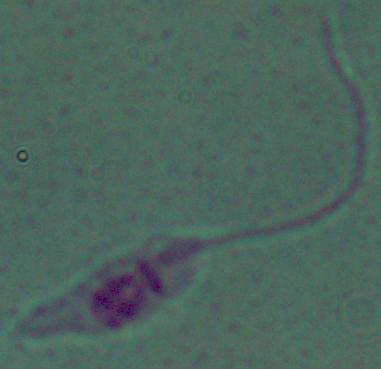
Captured at 1000x magnification. A Leishmania parasite is seen. Photomicrograph.